Point out each Plasmodium parasite and each leukocyte.
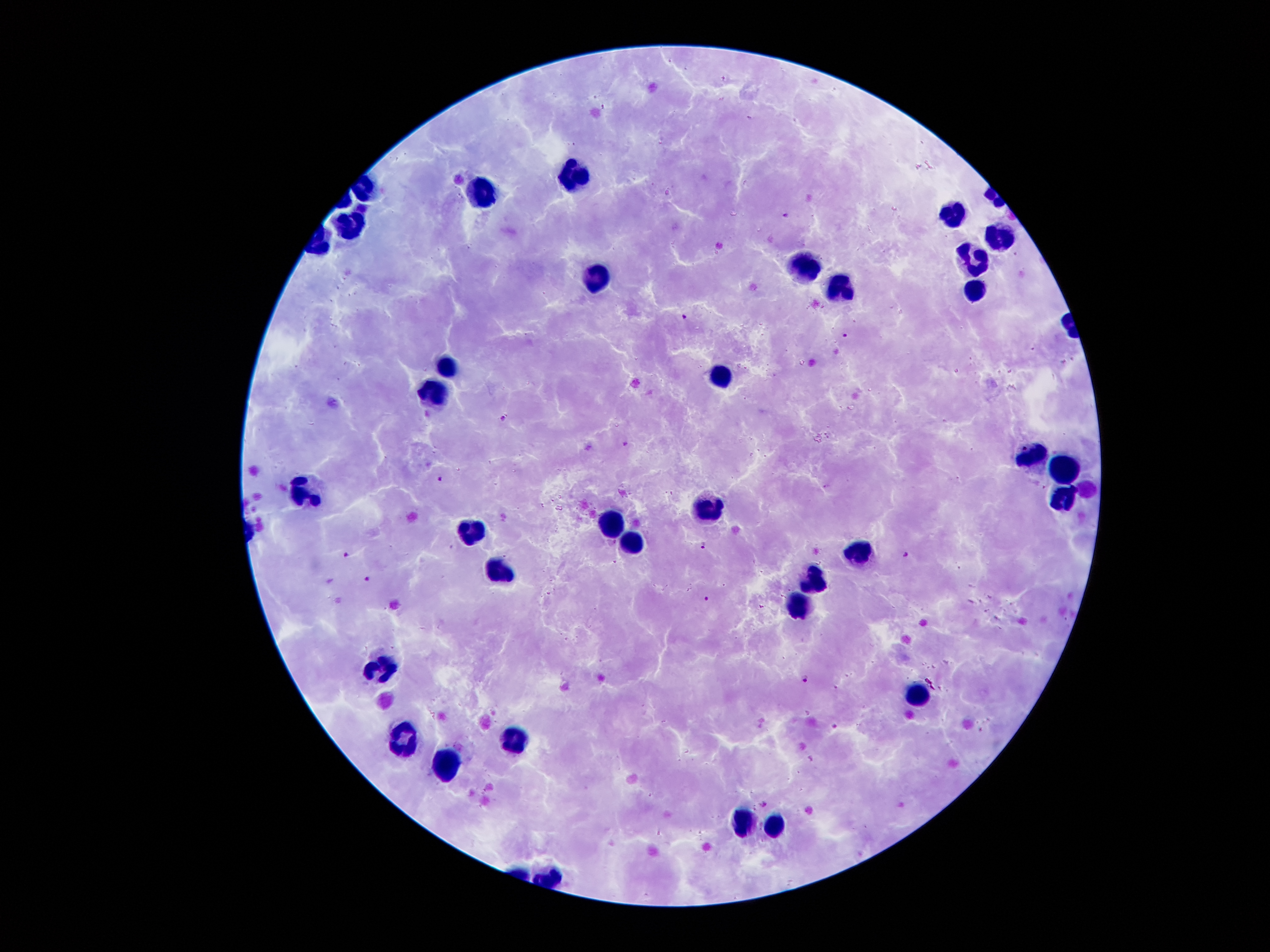
Approximate centers as [x, y] in pixels.
Plasmodium parasites: [603, 107], [784, 215], [683, 316], [845, 334], [503, 418], [625, 442], [441, 479], [702, 545], [346, 553], [906, 554], [366, 578], [707, 599], [805, 680], [836, 727], [764, 804].
Leukocytes: [573, 171], [481, 191], [952, 217], [351, 226], [1000, 238], [973, 260], [808, 266], [599, 276], [978, 291], [840, 293], [450, 366], [721, 375], [434, 395], [1034, 454], [1064, 467], [298, 493], [1063, 496], [709, 509], [609, 523], [470, 533], [636, 546], [860, 551], [501, 572], [814, 580], [799, 603], [385, 666], [918, 691], [517, 740], [402, 742], [447, 768], [741, 822], [774, 824].

{
  "stain": "Giemsa",
  "image_size": "1270×952 pixels",
  "preparation": "thick blood smear",
  "capture": "smartphone through the microscope eyepiece",
  "field_of_view": "single",
  "magnification": "100x",
  "patient_malaria_status": "positive for Plasmodium falciparum"
}